Name the parasite shown.
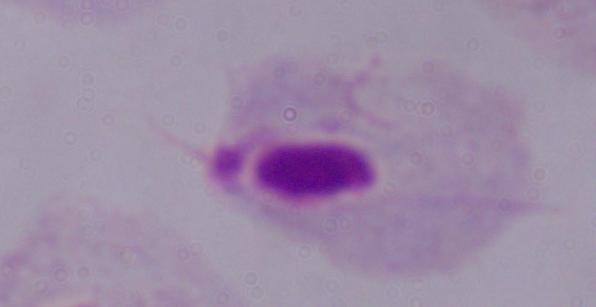
A trichomonad.

Micrograph. Captured at 1000x magnification.